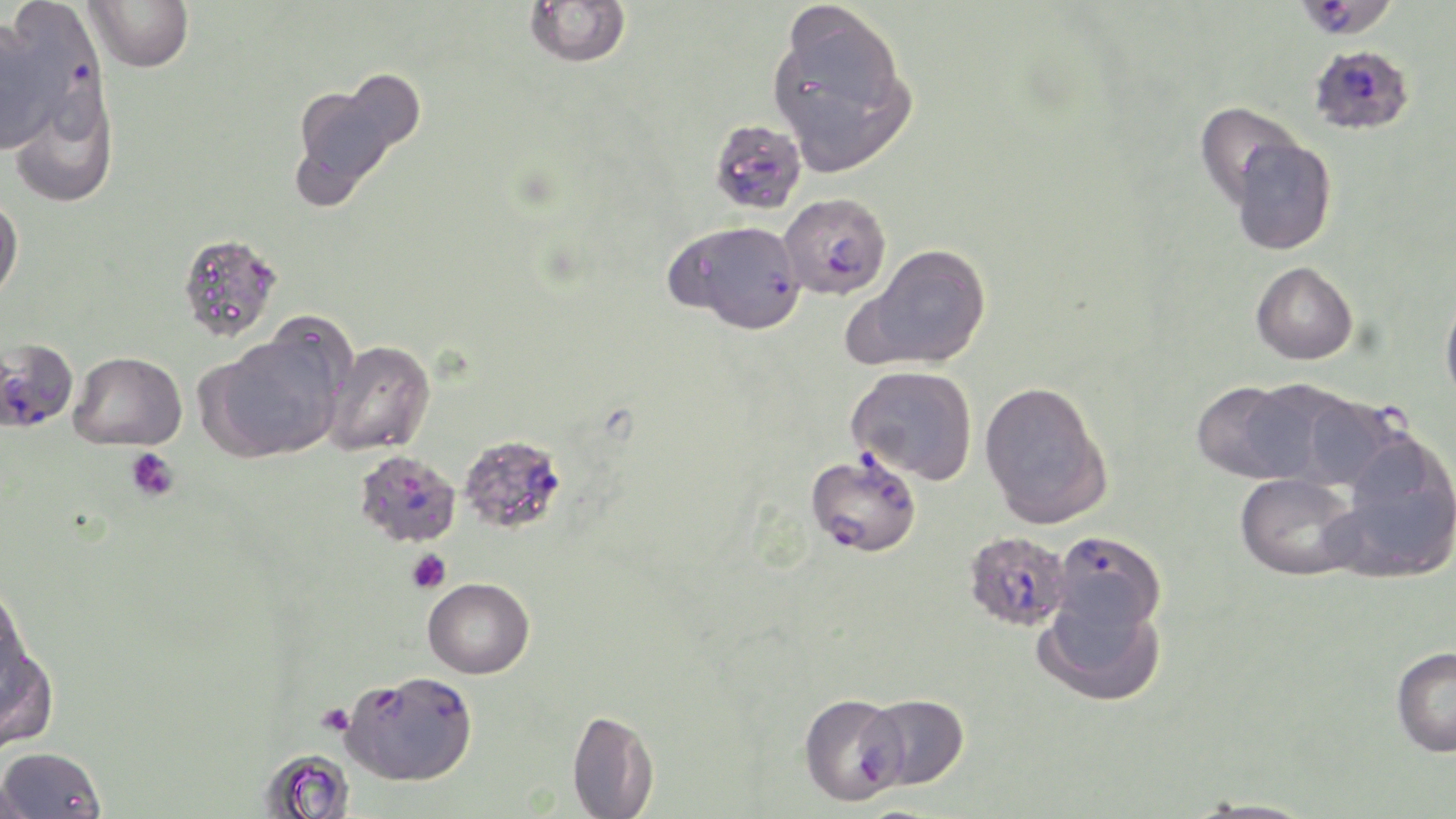

Summary:
  - Coordinate format: approximate bounding boxes as [x1, y1, x2, y2] in pixels
  - Uninfected red blood cell locations: [85, 0, 194, 71], [525, 1, 630, 67], [767, 6, 915, 173], [0, 20, 60, 154], [342, 68, 426, 152], [290, 82, 403, 202], [9, 93, 118, 208], [1194, 100, 1313, 215], [1227, 136, 1337, 255], [0, 197, 23, 303], [177, 232, 283, 342], [852, 243, 993, 370], [1250, 261, 1358, 365], [1440, 290, 1456, 408], [207, 331, 346, 461], [323, 340, 435, 456], [69, 351, 187, 450], [846, 365, 978, 484], [978, 380, 1113, 529], [1191, 381, 1316, 484], [1327, 433, 1456, 583], [1235, 473, 1362, 580], [423, 577, 534, 679], [0, 582, 34, 703], [1034, 590, 1166, 707], [0, 637, 58, 753], [1391, 646, 1456, 757], [798, 693, 908, 805], [566, 709, 660, 817], [0, 746, 107, 818], [258, 749, 356, 819], [0, 774, 36, 819], [1182, 797, 1323, 819]
  - Plasmodium falciparum-infected red blood cell locations: [39, 22, 110, 146], [1308, 43, 1415, 136], [709, 119, 807, 215], [778, 192, 891, 300], [670, 220, 807, 334], [0, 343, 77, 437], [1271, 393, 1428, 492], [457, 433, 568, 535], [353, 450, 461, 548], [806, 451, 922, 557], [1050, 530, 1166, 634], [963, 531, 1072, 632], [341, 671, 477, 785], [863, 693, 969, 789]
  - Platelet locations: [126, 447, 180, 502], [406, 548, 451, 594]
  - Slide-level diagnosis: Plasmodium falciparum
  - Magnification: 1000x
  - Preparation: thin blood smear
  - Field of view: one of a larger specimen
  - Image size: 1456×819 pixels
  - Stain: May-Grünwald-Giemsa
  - Modality: optical microscopy